Comment on the morphology of the erythrocytes.
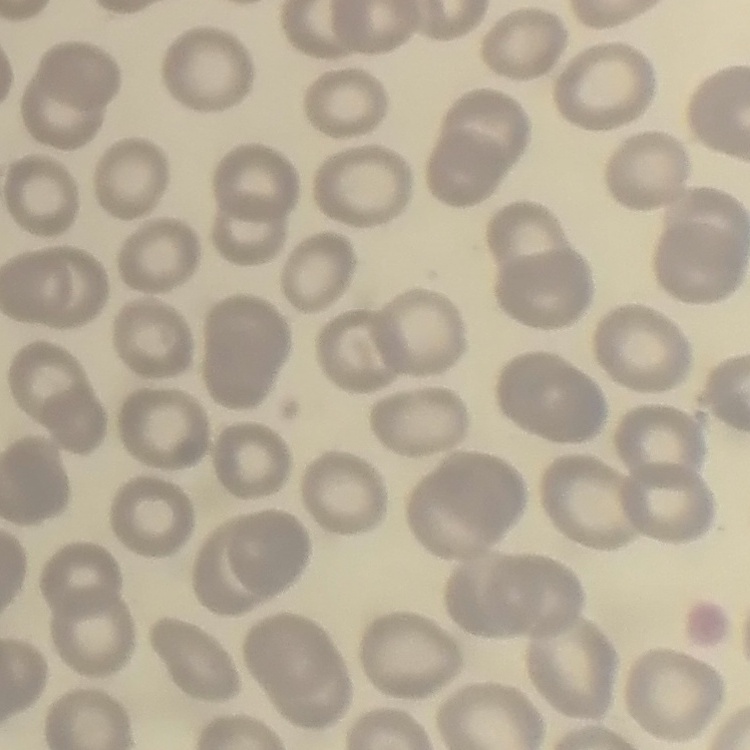

They show no rouleaux formation.

Summary:
  - Preparation: thin blood film
  - Stain: Field's or Giemsa
  - Image type: square crop of a larger photomicrograph